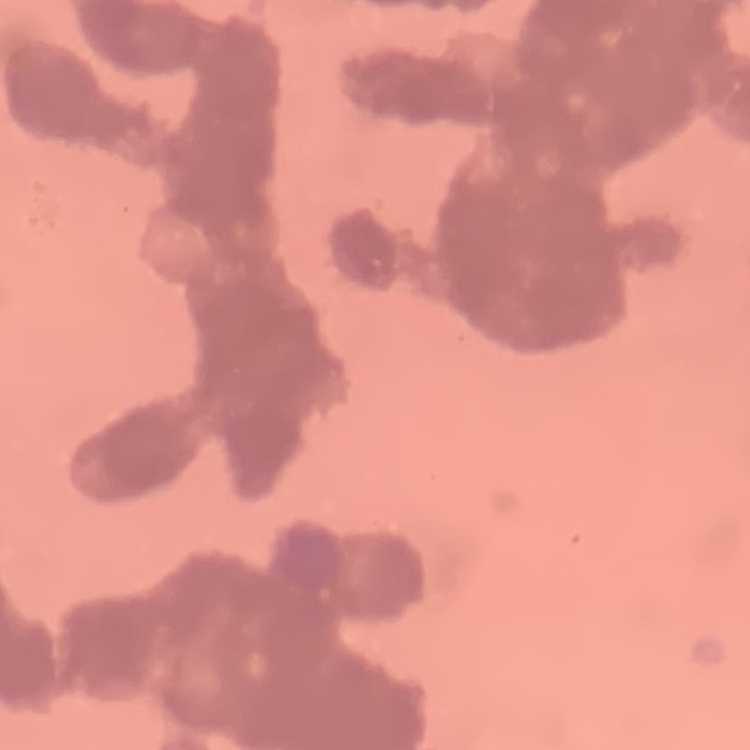
The erythrocytes exhibit rouleaux formation. One tile cut from a larger photomicrograph. Stained with either Field's or Giemsa. Thin peripheral smear.